Give the position of every Plasmodium parasite.
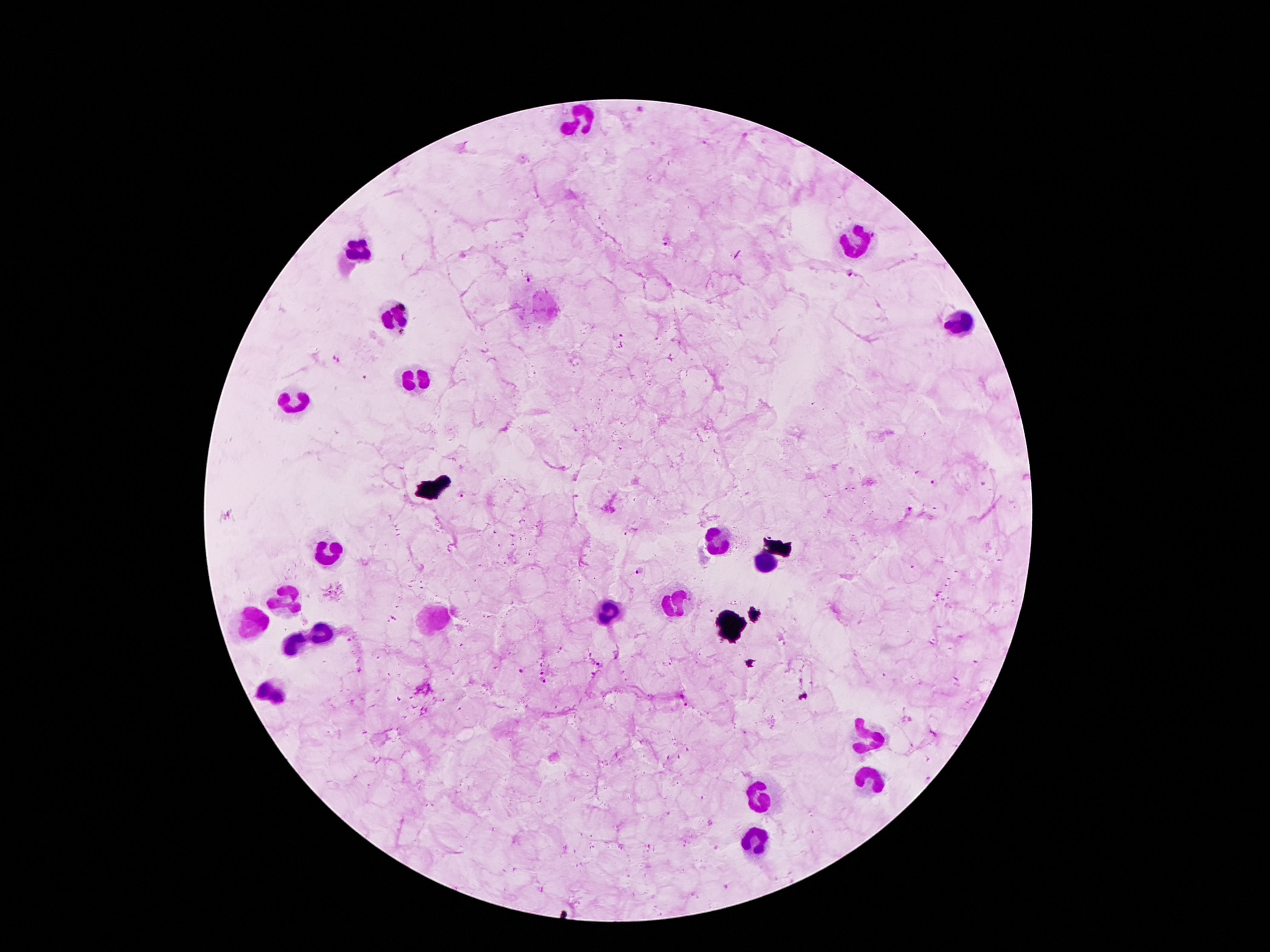
Approximate object centers, in pixels from the top-left corner.
Plasmodium parasites: (x=641, y=110), (x=668, y=240), (x=852, y=273), (x=528, y=277), (x=336, y=360), (x=934, y=484), (x=459, y=493), (x=630, y=532), (x=640, y=572), (x=601, y=666), (x=521, y=670), (x=544, y=671), (x=542, y=681).

Leukocyte locations: (x=585, y=120), (x=857, y=242), (x=358, y=250), (x=546, y=304), (x=393, y=316), (x=956, y=321), (x=419, y=377), (x=302, y=403), (x=719, y=541), (x=330, y=549), (x=763, y=563), (x=284, y=599), (x=676, y=604), (x=604, y=612), (x=254, y=624), (x=427, y=624), (x=317, y=633), (x=297, y=642), (x=274, y=689), (x=869, y=737), (x=872, y=778), (x=762, y=796), (x=755, y=843). Photographed through the microscope eyepiece with a smartphone camera. 100x magnification. Patient malaria status: infected with Plasmodium falciparum. Thick blood film. Giemsa-stained preparation. Single field of view. Image is 1270×952 pixels.